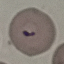
result = malaria parasites detected
capture = smartphone camera at the microscope eyepiece
preparation = thin blood film
stain = Giemsa
image type = automatically extracted cell patch, resized to 64 × 64 pixels